Assess this cell for malaria.
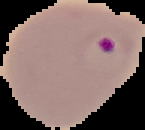
Parasitized.

Summary:
  - Preparation: thin blood smear
  - Image type: cell region segmented out of the field of view; surrounding area masked to black
  - Image size: 145×130 pixels